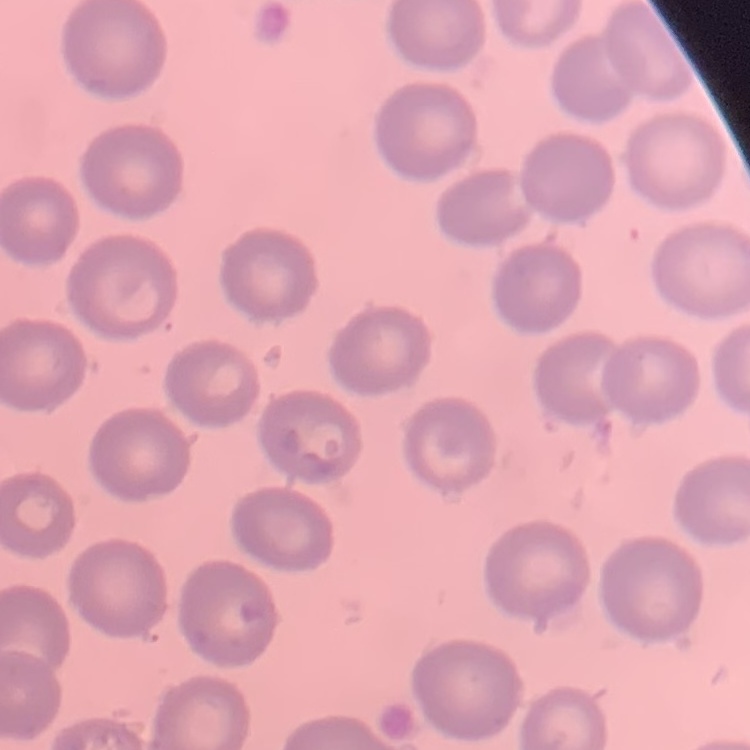
red blood cell morphology = no rouleaux formation
preparation = thin blood film
stain = Field's or Giemsa
image type = square crop of a larger photomicrograph